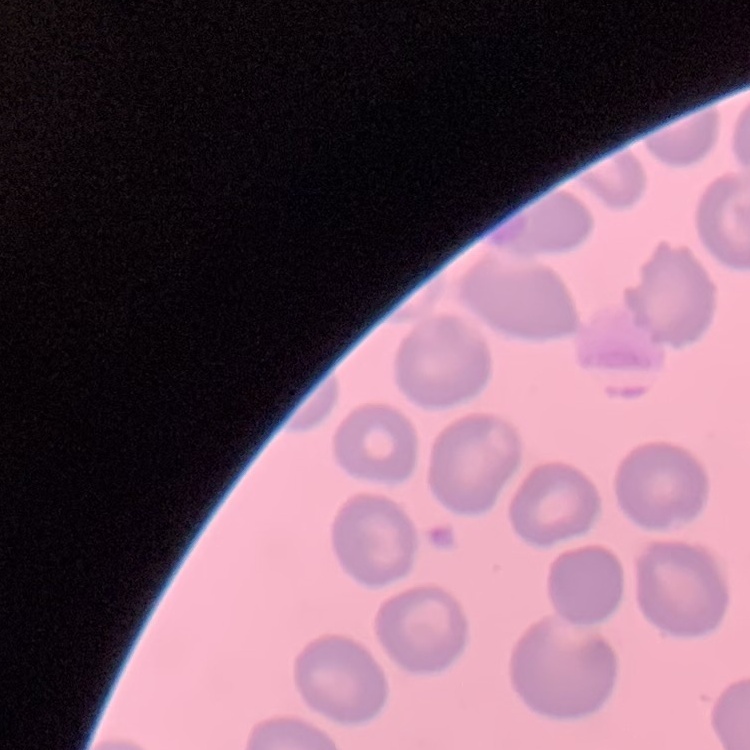
Summary:
  - Red blood cell morphology: no rouleaux formation
  - Preparation: thin peripheral smear
  - Image type: one tile cut from a larger photomicrograph
  - Stain: Field's or Giemsa